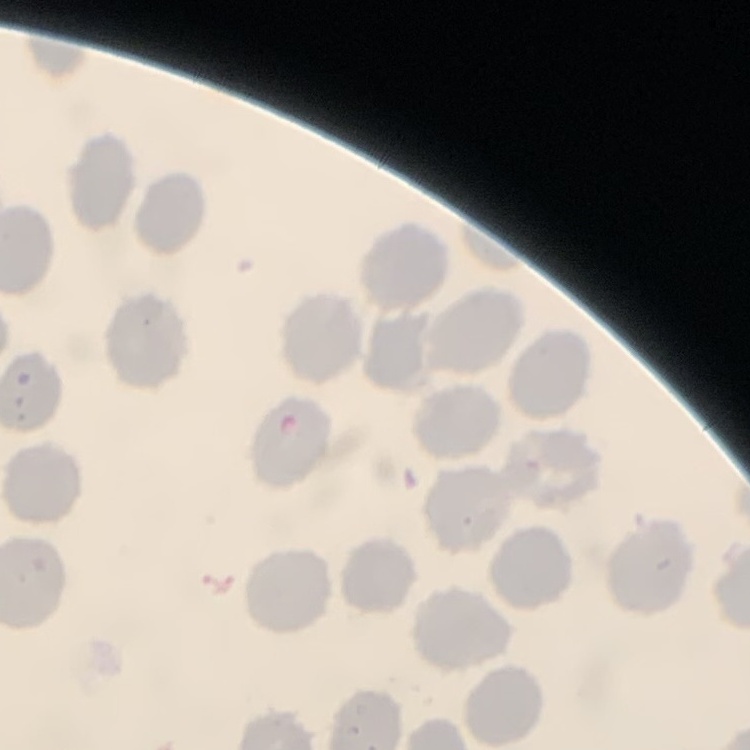

red blood cell morphology = no rouleaux formation
stain = Field's or Giemsa
preparation = thin blood smear
image type = square crop of a larger photomicrograph